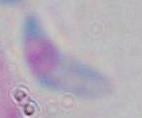

{
  "magnification": "1000x",
  "identification": "Toxoplasma gondii",
  "modality": "micrograph"
}